Name the blood parasite species.
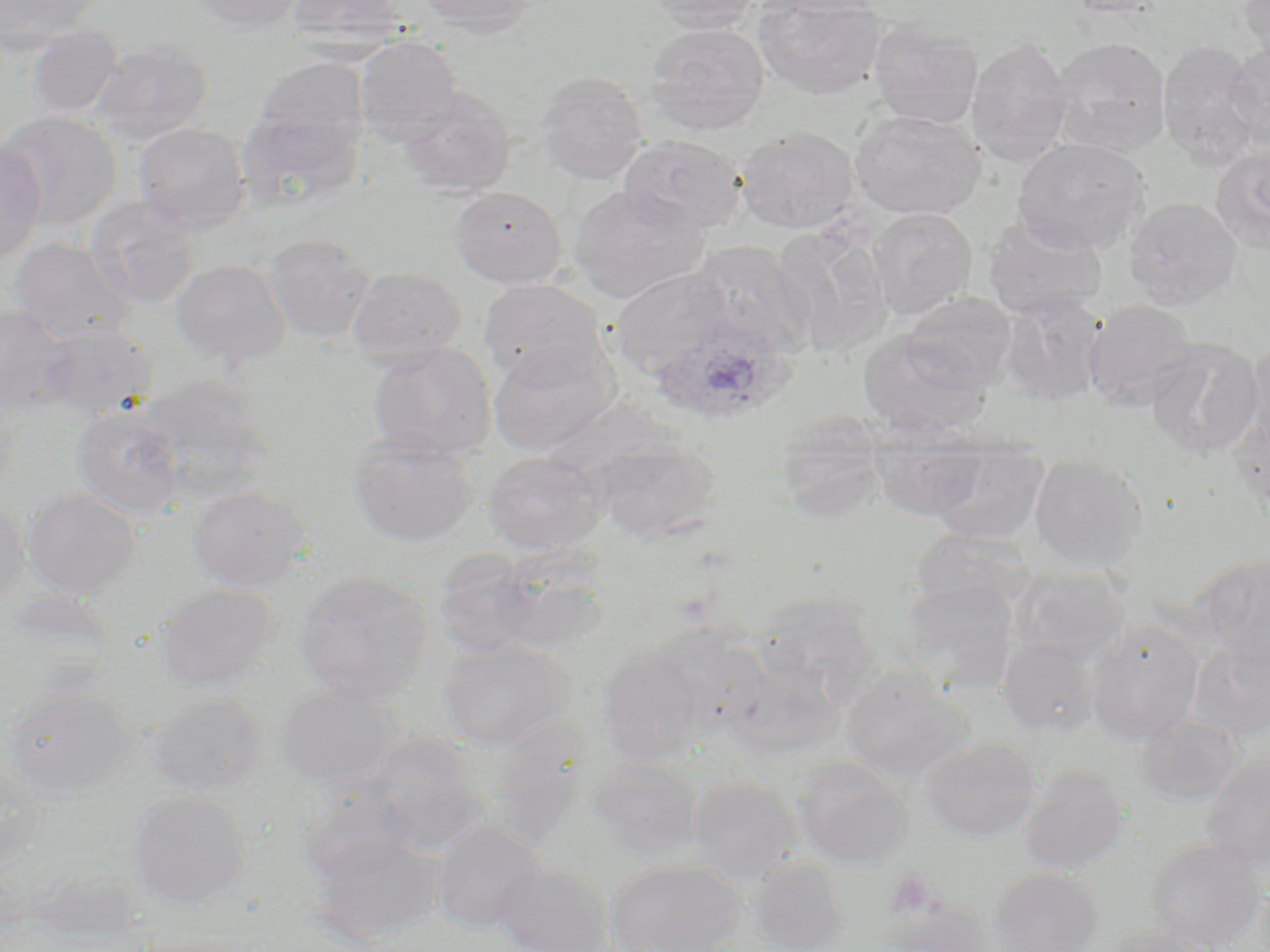

Plasmodium ovale.

magnification = 1000x
Plasmodium ovale-infected red blood cell locations = approximate bounding boxes as (x1,y1)-(x2,y2) corner pairs in pixels: (653,321)-(796,425)
image size = 1270×952 pixels
field of view = single
platelet locations = approximate bounding boxes as (x1,y1)-(x2,y2) corner pairs in pixels: (884,869)-(940,918)
stain = May-Grünwald-Giemsa
modality = light microscopy
preparation = thin blood smear
uninfected red blood cell locations = approximate bounding boxes as (x1,y1)-(x2,y2) corner pairs in pixels: (0,0)-(101,51), (189,0)-(307,32), (287,0)-(405,49), (414,0)-(541,36), (647,0)-(763,33), (1238,0)-(1269,66), (753,1)-(886,99), (867,19)-(984,130), (646,22)-(769,134), (27,24)-(123,118), (355,36)-(462,147), (966,38)-(1074,165), (1049,38)-(1172,158), (1224,39)-(1270,144), (89,40)-(213,146), (1156,40)-(1261,165), (250,58)-(370,167), (536,70)-(648,184), (398,86)-(516,198), (234,104)-(362,211), (2,109)-(122,231), (849,109)-(986,221), (133,122)-(251,234), (734,125)-(860,234), (618,134)-(747,235), (1013,137)-(1149,254), (0,142)-(48,265), (1211,146)-(1270,252), (568,185)-(708,303), (450,186)-(566,287), (87,196)-(201,310), (1124,197)-(1242,309), (867,208)-(978,319), (983,213)-(1108,320), (770,225)-(892,355), (260,233)-(377,345), (7,236)-(136,343), (688,240)-(816,358), (171,260)-(291,367), (609,266)-(732,379), (346,267)-(467,368), (479,279)-(608,385), (997,290)-(1107,406), (900,292)-(1018,391), (1083,299)-(1198,411), (0,305)-(77,417), (39,325)-(157,419), (857,330)-(991,436), (1145,337)-(1264,458), (1243,339)-(1270,459), (488,340)-(620,457), (366,341)-(497,461), (136,374)-(272,498), (0,386)-(23,500), (71,405)-(186,520), (772,414)-(890,526), (1230,414)-(1270,515), (867,426)-(993,519), (347,431)-(480,547), (590,435)-(723,543), (921,440)-(1049,543), (482,451)-(608,555), (1029,453)-(1148,571), (187,485)-(312,592), (22,487)-(142,600), (0,496)-(29,610), (909,527)-(1036,614), (432,548)-(546,658), (484,552)-(615,656), (1193,554)-(1270,665), (1011,565)-(1131,665), (291,570)-(434,703), (900,578)-(1020,696), (156,584)-(277,691), (751,595)-(883,712), (1084,621)-(1204,745), (998,638)-(1099,737), (437,639)-(575,751), (1188,641)-(1270,743), (596,643)-(720,766), (720,644)-(850,759), (840,666)-(972,783), (275,686)-(403,788), (2,688)-(140,800), (145,692)-(267,798), (1135,713)-(1246,808), (360,731)-(489,853), (921,736)-(1042,843), (1199,751)-(1270,870), (791,756)-(913,869), (586,758)-(705,857), (0,759)-(49,872), (1017,770)-(1131,878), (685,777)-(802,882), (295,779)-(419,885), (127,790)-(250,911), (430,820)-(547,934), (305,831)-(443,946), (1145,839)-(1267,952), (744,856)-(850,952), (604,859)-(747,952), (493,863)-(615,952), (986,867)-(1104,951), (25,869)-(147,942), (884,902)-(996,952), (1095,925)-(1220,952)